Name the cell type shown.
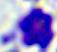
A leukocyte.

magnification = 400x
modality = micrograph